Describe the morphology of the red blood cells.
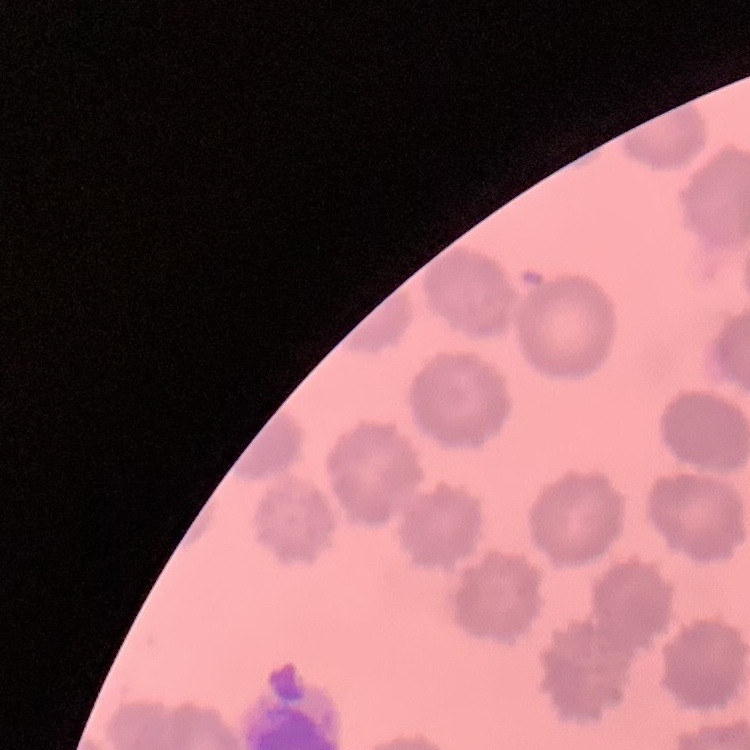
No rouleaux formation.

Summary:
  - Preparation: thin blood film
  - Stain: Field's or Giemsa
  - Image type: one tile cut from a larger photomicrograph